Point out each Plasmodium parasite and each leukocyte.
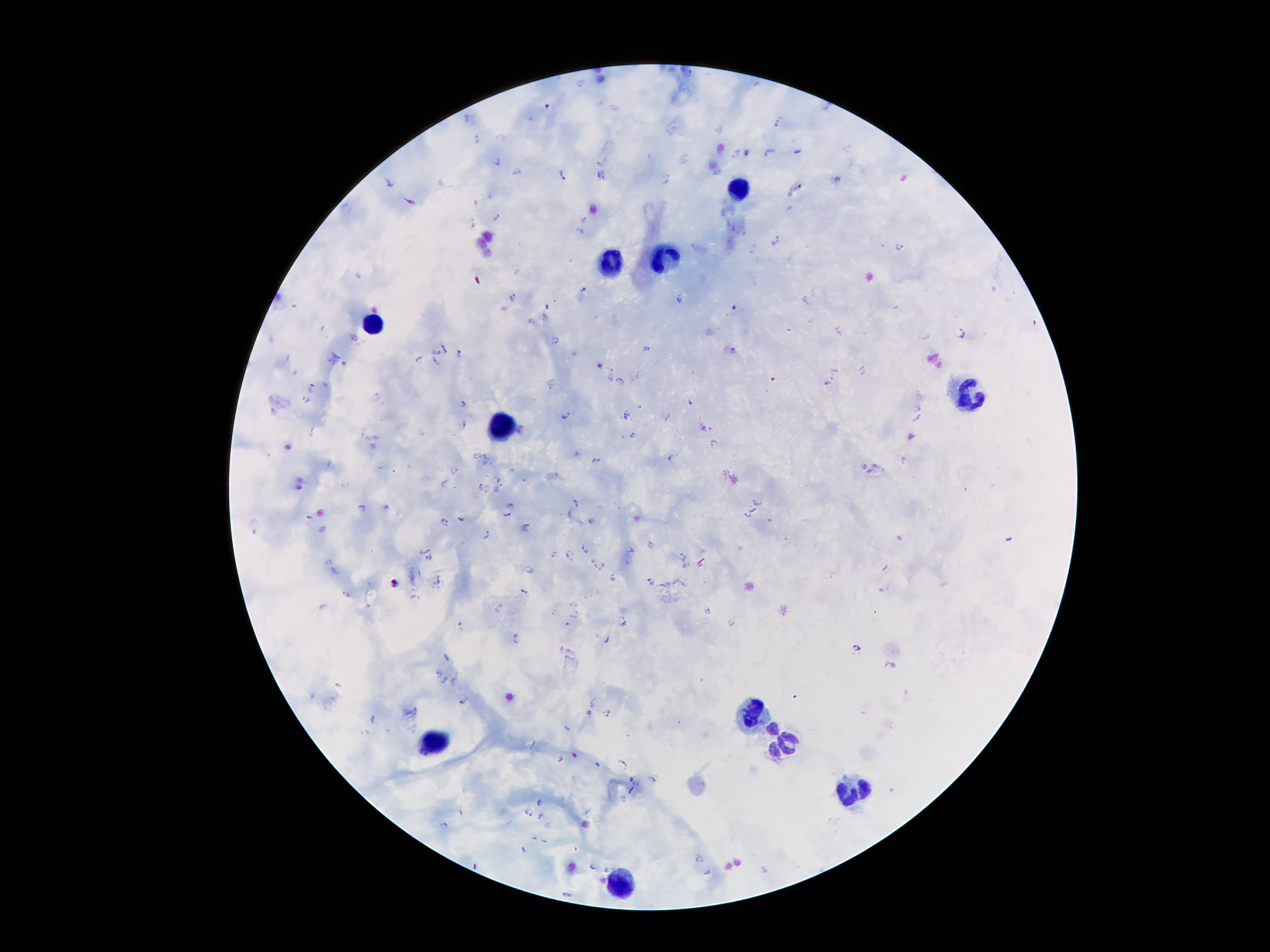
Approximate centers as [x, y] in pixels.
Plasmodium parasites (subset; some too small to resolve): [580, 83], [777, 118], [719, 127], [477, 138], [799, 151], [745, 152], [769, 152], [736, 153], [682, 159], [497, 161], [515, 171], [563, 172], [716, 173], [601, 174], [665, 178], [388, 182], [797, 187], [409, 201], [497, 217], [584, 219], [472, 223], [737, 228], [579, 232], [776, 242], [898, 247], [753, 250], [516, 272], [583, 290], [512, 296], [806, 301], [682, 302], [734, 306], [531, 320], [840, 330], [353, 335], [961, 335], [555, 337], [443, 347], [646, 349], [733, 351], [438, 352], [459, 353], [420, 358], [435, 360], [342, 362], [611, 368], [862, 370], [620, 380], [826, 382], [313, 385], [377, 393], [306, 398], [691, 401], [462, 402], [625, 415], [566, 416], [917, 419], [464, 424], [313, 428], [633, 436], [713, 442], [669, 458], [903, 458], [595, 459], [329, 463], [864, 466], [456, 469], [725, 472], [498, 479], [443, 482], [482, 488], [497, 488], [576, 501], [759, 503], [511, 504], [363, 507], [751, 510], [508, 514], [309, 516], [748, 517], [460, 518], [446, 520], [252, 524], [527, 526], [486, 535], [897, 536], [651, 544], [584, 548], [631, 549], [425, 550], [555, 552], [569, 553], [684, 556], [430, 557], [592, 559], [330, 561], [700, 563], [603, 565], [887, 567], [613, 578], [438, 580], [650, 582], [882, 588], [525, 590], [347, 594], [413, 596], [575, 603], [323, 607], [500, 607], [708, 611], [554, 612], [575, 615], [622, 620], [732, 622], [566, 623], [517, 637], [604, 642], [857, 647], [446, 658], [438, 670], [444, 679], [453, 681], [462, 701], [591, 703], [588, 713], [605, 713], [372, 719], [566, 727], [575, 755], [561, 759], [623, 762], [597, 764], [632, 779], [653, 779], [632, 789], [624, 798], [539, 802], [530, 810], [542, 816], [699, 856], [591, 865], [707, 871], [564, 893].
Leukocytes: [741, 191], [663, 256], [612, 264], [373, 319], [971, 394], [501, 427], [754, 713], [432, 741], [785, 741], [858, 790].

Image is 1270×952 pixels. Smartphone photograph taken through the microscope eyepiece. 100x magnification. Patient malaria status: infected with Plasmodium falciparum. Single field of view. Thick blood film. Giemsa stain.